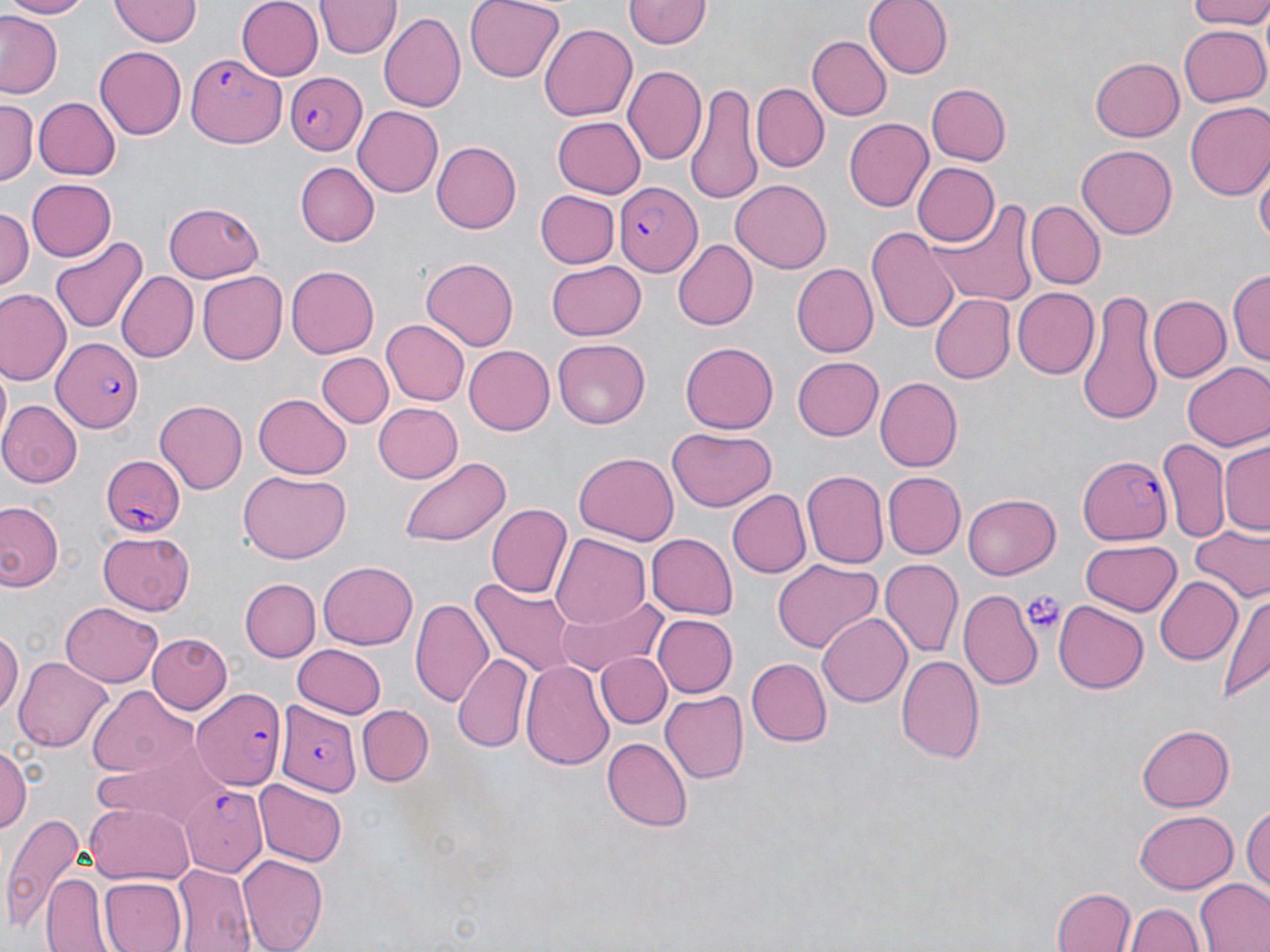
{
  "slide_level_diagnosis": "Plasmodium falciparum",
  "stain": "May-Grünwald-Giemsa",
  "magnification": "1000x",
  "modality": "light microscopy",
  "image_size": "1270×952 pixels",
  "field_of_view": "one of a larger specimen",
  "plasmodium_falciparum_infected_red_blood_cell_locations": "approximate bounding boxes as [x1, y1, x2, y2] in pixels: [185, 50, 288, 147], [283, 70, 368, 154], [614, 184, 702, 276], [52, 336, 144, 433], [1079, 453, 1173, 545], [99, 458, 187, 536], [194, 688, 283, 790], [278, 702, 359, 795], [183, 788, 267, 876]",
  "preparation": "thin blood smear",
  "uninfected_red_blood_cell_locations": "approximate bounding boxes as [x1, y1, x2, y2] in pixels: [0, 0, 90, 18], [110, 0, 199, 46], [235, 0, 322, 79], [465, 0, 565, 83], [865, 0, 950, 78], [1184, 0, 1270, 29], [318, 1, 400, 59], [624, 1, 709, 50], [377, 11, 465, 114], [0, 14, 65, 100], [540, 23, 639, 122], [1179, 26, 1269, 107], [806, 35, 890, 119], [94, 47, 186, 140], [1090, 57, 1184, 141], [625, 65, 706, 164], [750, 83, 827, 172], [926, 83, 1011, 166], [686, 84, 761, 204], [0, 97, 37, 186], [32, 98, 119, 180], [1184, 103, 1270, 202], [354, 105, 444, 198], [550, 115, 645, 198], [845, 117, 936, 212], [430, 141, 521, 233], [1077, 146, 1177, 239], [296, 163, 379, 246], [912, 163, 999, 247], [1256, 166, 1269, 249], [24, 178, 116, 262], [731, 181, 831, 273], [535, 190, 619, 268], [165, 199, 265, 282], [925, 199, 1039, 312], [1028, 200, 1104, 290], [0, 206, 33, 298], [868, 227, 958, 336], [48, 235, 145, 336], [673, 240, 756, 330], [418, 257, 519, 352], [547, 258, 646, 338], [790, 263, 877, 358], [284, 264, 377, 359], [1229, 268, 1270, 366], [197, 270, 288, 365], [114, 272, 197, 364], [1076, 285, 1163, 429], [1, 288, 69, 386], [1012, 288, 1097, 377], [931, 294, 1014, 384], [1147, 294, 1229, 384], [380, 320, 468, 407], [552, 338, 649, 429], [681, 341, 780, 433], [465, 344, 557, 434], [319, 353, 392, 427], [792, 357, 884, 441], [1182, 362, 1270, 452], [874, 378, 962, 472], [253, 390, 351, 478], [155, 400, 247, 493], [0, 401, 80, 488], [373, 401, 462, 484], [669, 428, 775, 511], [1160, 437, 1230, 542], [1221, 440, 1270, 537], [573, 453, 678, 544], [399, 456, 510, 548], [804, 470, 888, 570], [236, 471, 349, 564], [885, 472, 965, 558], [725, 489, 811, 579], [962, 493, 1061, 580], [0, 500, 64, 595], [487, 503, 574, 599], [1189, 527, 1269, 605], [98, 530, 197, 616], [646, 533, 737, 619], [550, 535, 650, 631], [1081, 540, 1181, 615], [880, 558, 962, 659], [772, 559, 880, 652], [318, 561, 419, 650], [1154, 575, 1243, 664], [239, 578, 319, 662], [470, 578, 577, 676], [960, 588, 1044, 690], [1220, 590, 1270, 704], [410, 592, 495, 708], [554, 596, 667, 675], [1052, 600, 1150, 695], [59, 603, 163, 687], [816, 613, 910, 707], [651, 614, 736, 698], [0, 630, 21, 720], [147, 632, 231, 712], [292, 645, 386, 719], [593, 652, 669, 728], [454, 653, 534, 751], [897, 653, 986, 766], [15, 657, 111, 755], [519, 657, 614, 768], [747, 658, 833, 747], [88, 686, 195, 778], [660, 689, 750, 785], [357, 704, 432, 785], [1136, 724, 1234, 811], [100, 730, 229, 831], [602, 738, 691, 831], [0, 743, 31, 839], [253, 779, 347, 867], [85, 800, 193, 885], [1242, 803, 1270, 896], [2, 809, 84, 938], [1135, 810, 1235, 893], [238, 855, 328, 951], [173, 866, 256, 952], [46, 873, 110, 950], [96, 876, 185, 952], [1195, 878, 1270, 952], [1053, 888, 1136, 952], [1128, 904, 1202, 952]",
  "platelet_locations": "approximate bounding boxes as [x1, y1, x2, y2] in pixels: [1020, 590, 1065, 635]"
}